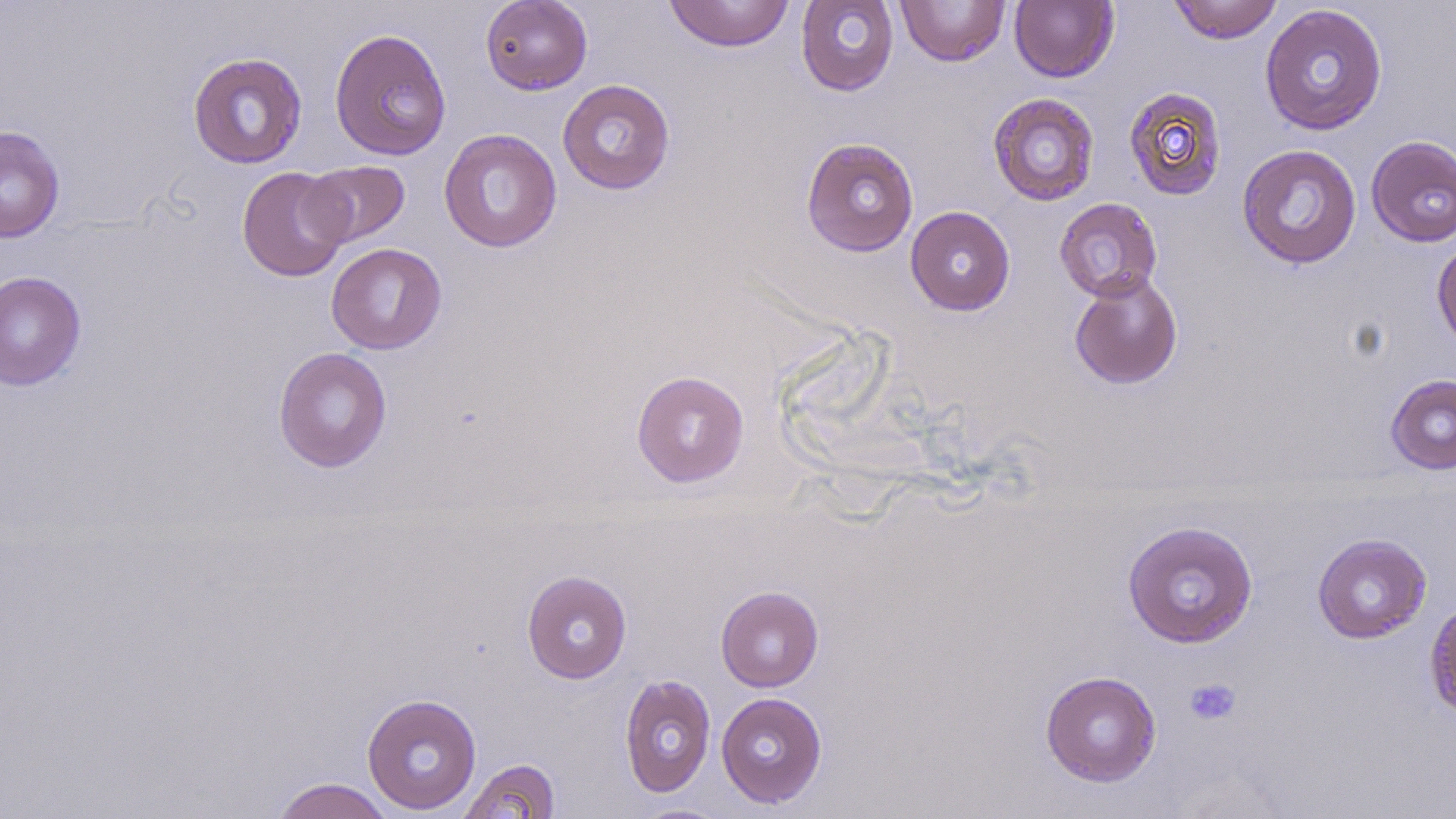

Summary:
  - Coordinate format: approximate bounding boxes as (x1, y1, x2, y2) in pixels
  - Uninfected red blood cell locations: (480, 0, 592, 95), (663, 0, 795, 52), (795, 0, 899, 96), (1009, 0, 1119, 83), (1168, 0, 1283, 44), (895, 1, 1011, 66), (1259, 3, 1388, 136), (329, 27, 452, 161), (187, 52, 308, 169), (558, 79, 675, 195), (1124, 86, 1227, 201), (987, 93, 1100, 206), (0, 125, 65, 244), (439, 128, 562, 253), (1365, 135, 1456, 247), (800, 137, 919, 257), (1237, 144, 1362, 269), (301, 160, 411, 248), (237, 166, 351, 282), (1054, 197, 1163, 302), (905, 205, 1015, 316), (1432, 238, 1456, 355), (326, 243, 446, 354), (0, 270, 86, 391), (1068, 271, 1183, 390), (273, 347, 392, 473), (631, 370, 749, 487), (1386, 374, 1456, 474), (1122, 519, 1258, 648), (1312, 533, 1432, 644), (521, 570, 632, 683), (716, 586, 824, 691), (1424, 598, 1456, 724), (1040, 670, 1161, 787), (619, 674, 716, 797), (716, 692, 828, 808), (362, 693, 482, 815), (458, 758, 560, 819), (270, 777, 395, 819), (632, 803, 733, 818)
  - Platelet locations: (1184, 677, 1241, 725)
  - Slide-level diagnosis: no evidence of blood parasites
  - Image size: 1456×819 pixels
  - Field of view: one of a larger specimen
  - Preparation: thin blood film
  - Modality: optical microscopy
  - Stain: May-Grünwald-Giemsa
  - Magnification: 1000x